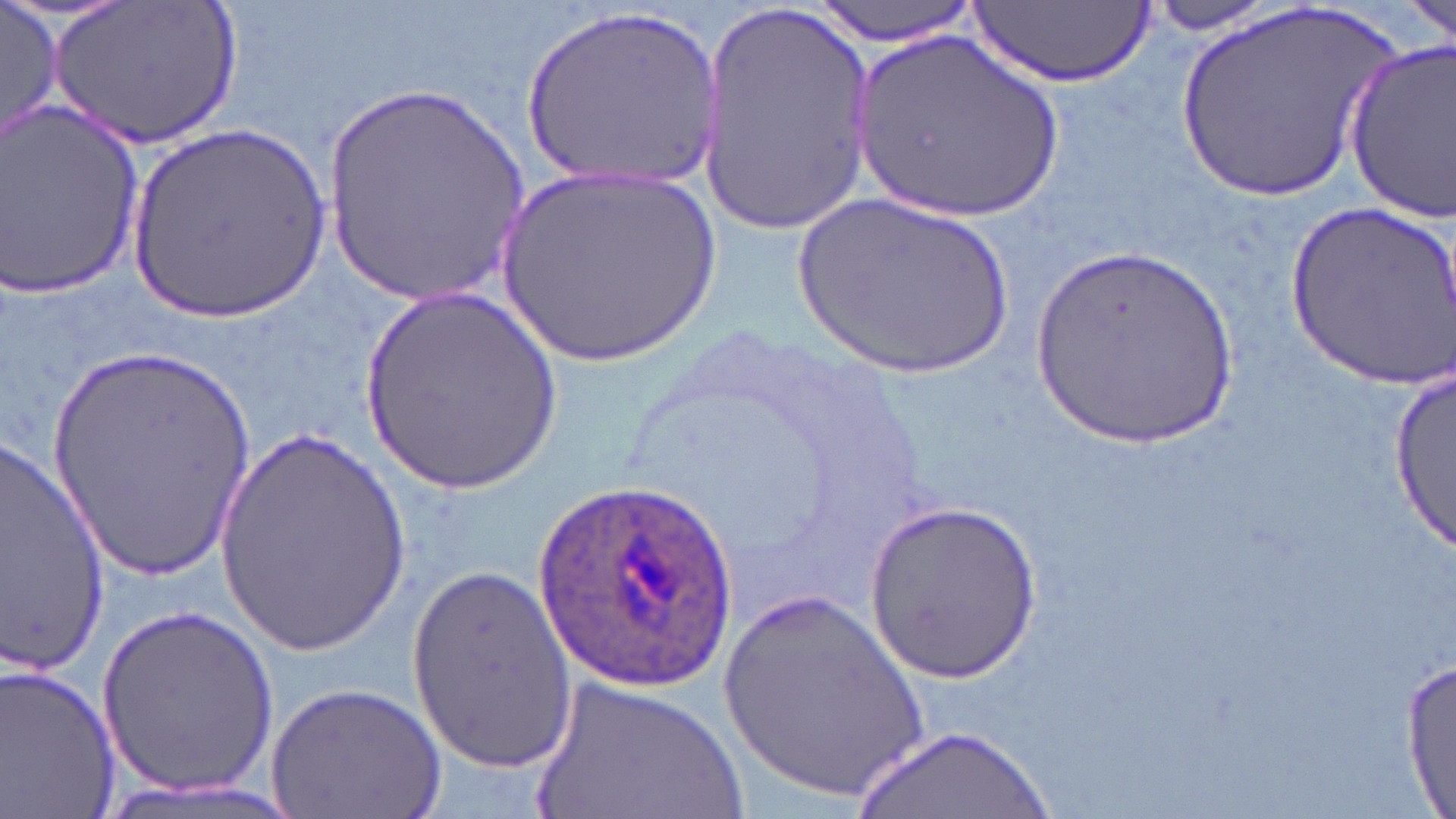
Approximate bounding boxes as [x1, y1, x2, y2] in pixels. Uninfected red blood cell locations: [2, 0, 62, 146], [49, 0, 237, 151], [807, 0, 984, 44], [1144, 0, 1297, 33], [1406, 0, 1455, 47], [971, 1, 1152, 87], [696, 4, 880, 232], [1171, 4, 1405, 210], [515, 5, 726, 196], [851, 30, 1069, 225], [1343, 38, 1456, 225], [319, 86, 530, 306], [2, 102, 148, 304], [126, 119, 335, 321], [491, 162, 724, 370], [786, 190, 1021, 385], [1287, 197, 1456, 389], [1028, 245, 1248, 454], [359, 284, 562, 499], [45, 343, 260, 586], [1391, 355, 1453, 560], [210, 422, 415, 657], [1, 430, 108, 677], [865, 498, 1041, 679], [406, 566, 576, 774], [715, 583, 934, 803], [100, 601, 278, 798], [1402, 660, 1455, 815], [0, 662, 123, 818], [527, 675, 753, 819], [263, 680, 446, 819], [856, 726, 1053, 819]. Plasmodium ovale-infected red blood cell locations: [534, 480, 740, 692]. Slide-level diagnosis: Plasmodium ovale. Single field of view. Light microscopy. Image is 1456×819 pixels. May-Grünwald-Giemsa-stained preparation. Thin blood smear. Captured at 1000x magnification.